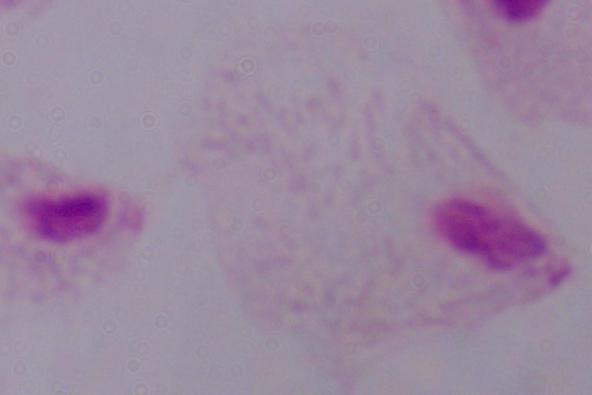

identification = trichomonad
magnification = 1000x
modality = micrograph